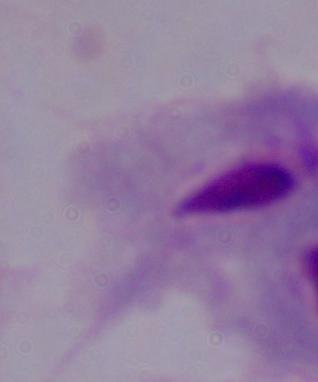

magnification = 1000x
modality = photomicrograph
identification = trichomonad